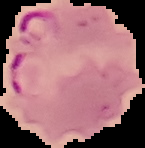

Cell region segmented out of the field of view; the surrounding area is masked to black. Malaria status: parasitized. Image is 145×148 pixels. From a thin blood smear.